Identify the blood parasite species.
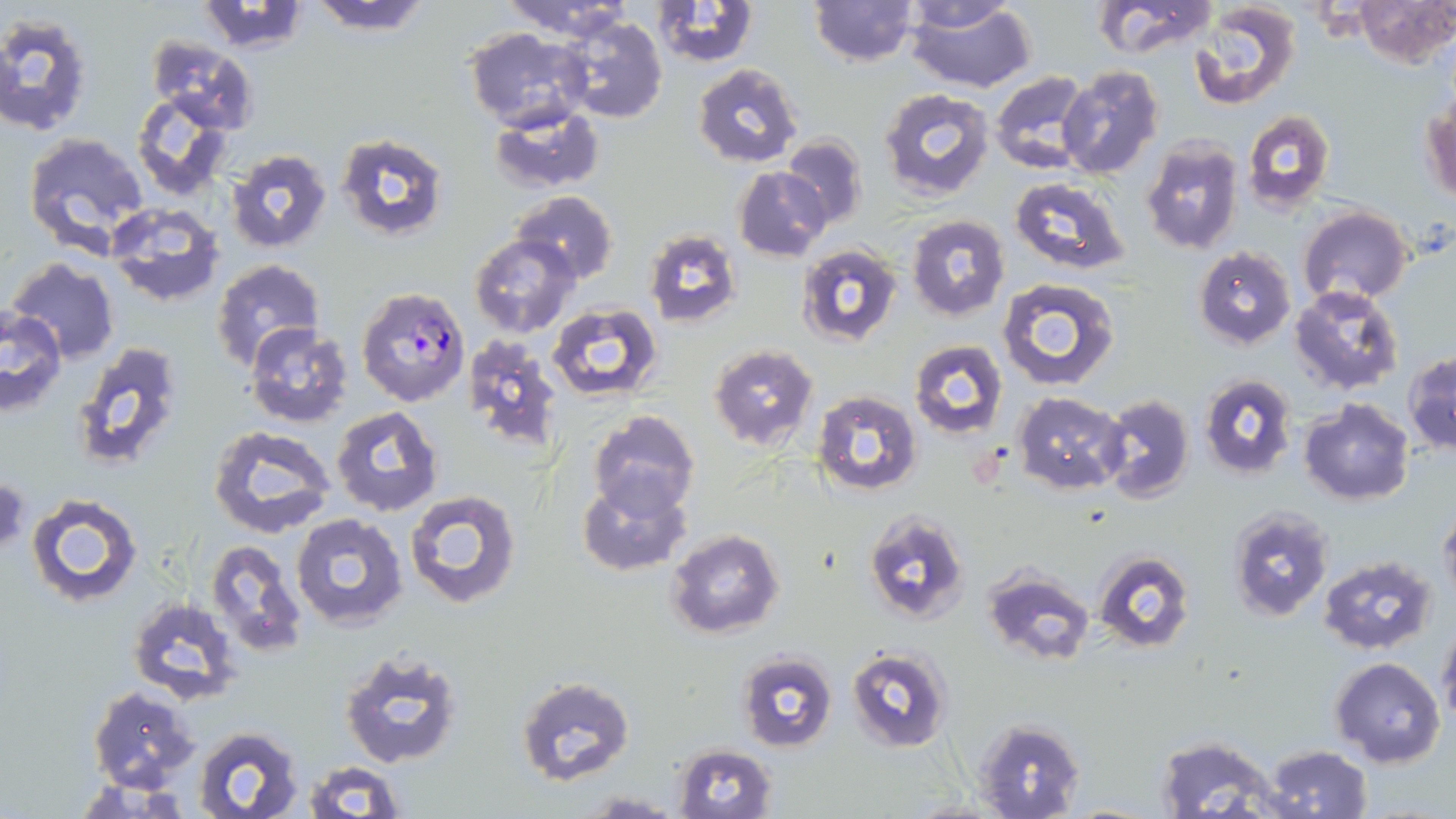
Plasmodium falciparum.

Summary:
  - Coordinate format: approximate bounding boxes as named x1/y1/x2/y2 corners in pixels
  - Uninfected red blood cell locations: (x1=305, y1=0, x2=433, y2=36), (x1=498, y1=0, x2=633, y2=40), (x1=650, y1=0, x2=760, y2=68), (x1=810, y1=0, x2=917, y2=67), (x1=903, y1=0, x2=1037, y2=93), (x1=1091, y1=0, x2=1218, y2=58), (x1=1356, y1=0, x2=1454, y2=67), (x1=196, y1=1, x2=310, y2=55), (x1=1188, y1=2, x2=1302, y2=110), (x1=0, y1=11, x2=95, y2=138), (x1=558, y1=16, x2=668, y2=126), (x1=462, y1=27, x2=590, y2=131), (x1=146, y1=36, x2=260, y2=132), (x1=691, y1=64, x2=802, y2=167), (x1=1056, y1=65, x2=1163, y2=178), (x1=988, y1=69, x2=1092, y2=173), (x1=878, y1=88, x2=994, y2=202), (x1=131, y1=91, x2=236, y2=201), (x1=488, y1=105, x2=604, y2=194), (x1=1422, y1=106, x2=1455, y2=203), (x1=1243, y1=110, x2=1335, y2=210), (x1=22, y1=131, x2=149, y2=254), (x1=335, y1=134, x2=448, y2=240), (x1=781, y1=134, x2=868, y2=231), (x1=1140, y1=136, x2=1243, y2=256), (x1=224, y1=147, x2=333, y2=255), (x1=733, y1=166, x2=830, y2=262), (x1=1008, y1=179, x2=1131, y2=274), (x1=510, y1=191, x2=618, y2=284), (x1=103, y1=202, x2=225, y2=309), (x1=1297, y1=207, x2=1414, y2=304), (x1=907, y1=215, x2=1009, y2=321), (x1=642, y1=229, x2=741, y2=329), (x1=468, y1=234, x2=578, y2=338), (x1=796, y1=242, x2=904, y2=348), (x1=1192, y1=248, x2=1297, y2=348), (x1=7, y1=256, x2=121, y2=363), (x1=209, y1=258, x2=324, y2=373), (x1=997, y1=276, x2=1122, y2=391), (x1=1291, y1=286, x2=1405, y2=397), (x1=547, y1=302, x2=663, y2=401), (x1=0, y1=307, x2=67, y2=415), (x1=245, y1=324, x2=353, y2=427), (x1=463, y1=335, x2=564, y2=454), (x1=909, y1=339, x2=1008, y2=440), (x1=70, y1=341, x2=185, y2=471), (x1=709, y1=344, x2=819, y2=451), (x1=1404, y1=352, x2=1456, y2=454), (x1=1199, y1=373, x2=1297, y2=480), (x1=811, y1=391, x2=922, y2=495), (x1=1098, y1=392, x2=1195, y2=502), (x1=1012, y1=393, x2=1128, y2=493), (x1=1300, y1=398, x2=1413, y2=505), (x1=331, y1=406, x2=443, y2=516), (x1=588, y1=410, x2=700, y2=520), (x1=208, y1=425, x2=337, y2=537), (x1=575, y1=473, x2=691, y2=578), (x1=1, y1=479, x2=28, y2=559), (x1=404, y1=489, x2=522, y2=609), (x1=27, y1=492, x2=142, y2=605), (x1=1439, y1=503, x2=1456, y2=612), (x1=1226, y1=507, x2=1338, y2=623), (x1=863, y1=509, x2=971, y2=628), (x1=291, y1=512, x2=408, y2=630), (x1=665, y1=530, x2=784, y2=641), (x1=205, y1=539, x2=308, y2=657), (x1=1092, y1=550, x2=1195, y2=654), (x1=1317, y1=554, x2=1437, y2=655), (x1=983, y1=566, x2=1092, y2=665), (x1=128, y1=596, x2=241, y2=705), (x1=1437, y1=623, x2=1456, y2=732), (x1=340, y1=648, x2=466, y2=770), (x1=846, y1=648, x2=952, y2=750), (x1=736, y1=650, x2=838, y2=751), (x1=1331, y1=657, x2=1446, y2=769), (x1=516, y1=677, x2=634, y2=784), (x1=88, y1=687, x2=200, y2=792), (x1=971, y1=717, x2=1085, y2=819), (x1=191, y1=726, x2=306, y2=819), (x1=1154, y1=735, x2=1281, y2=816), (x1=1263, y1=743, x2=1372, y2=818), (x1=670, y1=744, x2=779, y2=819), (x1=300, y1=761, x2=404, y2=818), (x1=581, y1=791, x2=682, y2=817)
  - Plasmodium falciparum-infected red blood cell locations: (x1=356, y1=286, x2=471, y2=407)
  - Preparation: thin blood film
  - Field of view: single
  - Magnification: 1000x
  - Stain: May-Grünwald-Giemsa
  - Image size: 1456×819 pixels
  - Modality: light microscopy